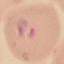
Summary:
  - Result: malaria parasites identified
  - Image type: automatically extracted cell patch, resized to 64 × 64 pixels
  - Preparation: thin smear
  - Stain: Giemsa
  - Capture: smartphone camera at the microscope eyepiece